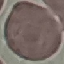
Malaria status: uninfected. Thin blood smear. Cell patch, automatically extracted from a larger field of view and resized to 64 × 64 pixels. Giemsa stain. Photographed with a smartphone camera at the microscope eyepiece.